Outline each blood parasite and name the species.
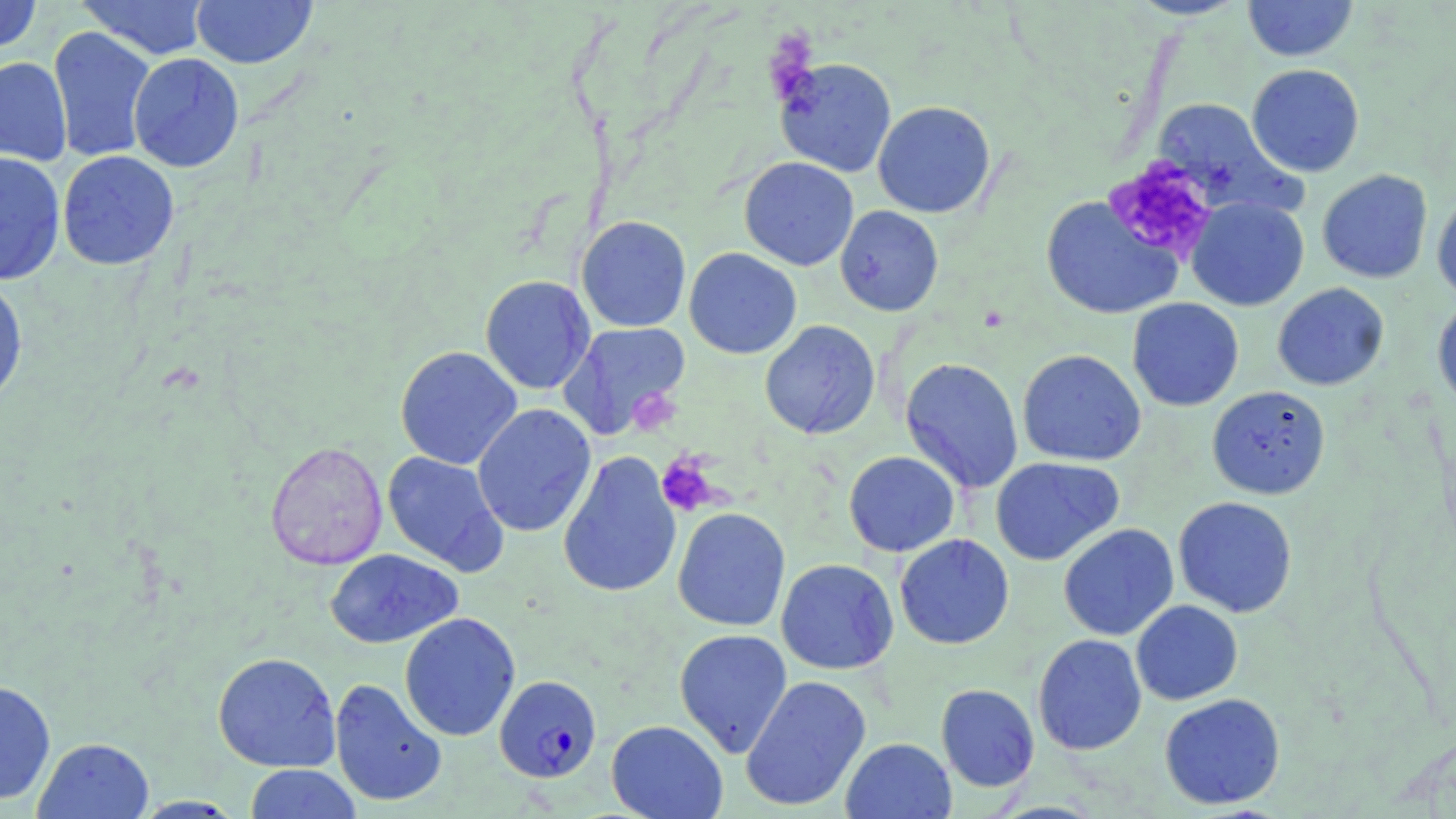
Approximate bounding boxes as named x1/y1/x2/y2 corners in pixels.
Plasmodium falciparum-infected red blood cells: (x1=494, y1=675, x2=602, y2=783).
No Plasmodium ovale, Plasmodium malariae, Plasmodium vivax, Babesia divergens, or Trypanosoma brucei observed.

slide-level diagnosis = Plasmodium falciparum
platelet locations = approximate bounding boxes as named x1/y1/x2/y2 corners in pixels: (x1=1103, y1=158, x2=1218, y2=263), (x1=656, y1=454, x2=719, y2=516)
preparation = thin blood film
image size = 1456×819 pixels
magnification = 1000x
modality = optical microscopy
field of view = one of a larger specimen
uninfected red blood cell locations = approximate bounding boxes as named x1/y1/x2/y2 corners in pixels: (x1=0, y1=0, x2=43, y2=54), (x1=76, y1=0, x2=211, y2=60), (x1=190, y1=0, x2=318, y2=69), (x1=1127, y1=0, x2=1249, y2=20), (x1=1242, y1=0, x2=1358, y2=62), (x1=47, y1=26, x2=157, y2=163), (x1=128, y1=53, x2=245, y2=173), (x1=0, y1=57, x2=73, y2=166), (x1=775, y1=57, x2=897, y2=178), (x1=1246, y1=64, x2=1365, y2=177), (x1=1151, y1=98, x2=1302, y2=218), (x1=872, y1=101, x2=996, y2=218), (x1=57, y1=150, x2=180, y2=270), (x1=0, y1=151, x2=66, y2=286), (x1=739, y1=156, x2=859, y2=271), (x1=1317, y1=169, x2=1433, y2=283), (x1=1432, y1=192, x2=1456, y2=304), (x1=1040, y1=196, x2=1183, y2=320), (x1=1187, y1=196, x2=1309, y2=311), (x1=835, y1=205, x2=944, y2=316), (x1=575, y1=215, x2=692, y2=333), (x1=684, y1=248, x2=801, y2=359), (x1=0, y1=275, x2=28, y2=411), (x1=480, y1=275, x2=595, y2=394), (x1=1272, y1=283, x2=1389, y2=391), (x1=1127, y1=298, x2=1244, y2=411), (x1=1432, y1=300, x2=1456, y2=413), (x1=759, y1=320, x2=880, y2=439), (x1=557, y1=321, x2=691, y2=440), (x1=395, y1=346, x2=522, y2=470), (x1=1017, y1=349, x2=1146, y2=466), (x1=900, y1=357, x2=1024, y2=493), (x1=1206, y1=385, x2=1330, y2=499), (x1=471, y1=403, x2=596, y2=537), (x1=265, y1=441, x2=388, y2=570), (x1=382, y1=451, x2=508, y2=576), (x1=558, y1=451, x2=682, y2=598), (x1=843, y1=451, x2=960, y2=557), (x1=990, y1=457, x2=1124, y2=566), (x1=1172, y1=496, x2=1297, y2=618), (x1=672, y1=507, x2=791, y2=632), (x1=1058, y1=524, x2=1179, y2=641), (x1=895, y1=534, x2=1014, y2=650), (x1=325, y1=548, x2=463, y2=648), (x1=775, y1=558, x2=899, y2=675), (x1=1131, y1=600, x2=1243, y2=705), (x1=399, y1=612, x2=521, y2=742), (x1=674, y1=628, x2=793, y2=757), (x1=1032, y1=633, x2=1147, y2=755), (x1=212, y1=651, x2=341, y2=773), (x1=740, y1=674, x2=872, y2=812), (x1=329, y1=677, x2=447, y2=807), (x1=0, y1=679, x2=56, y2=805), (x1=935, y1=684, x2=1040, y2=792), (x1=1159, y1=693, x2=1286, y2=810), (x1=606, y1=719, x2=728, y2=819), (x1=33, y1=737, x2=154, y2=819), (x1=841, y1=737, x2=956, y2=819), (x1=244, y1=764, x2=362, y2=819), (x1=131, y1=796, x2=246, y2=818)
stain = May-Grünwald-Giemsa